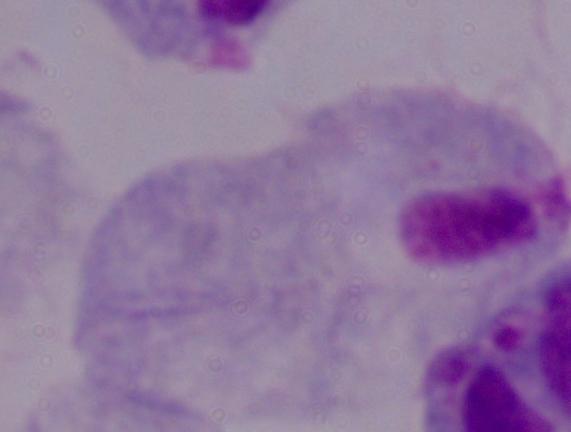

Micrograph. 1000x magnification. A trichomonad is shown.